Point out leukocytes.
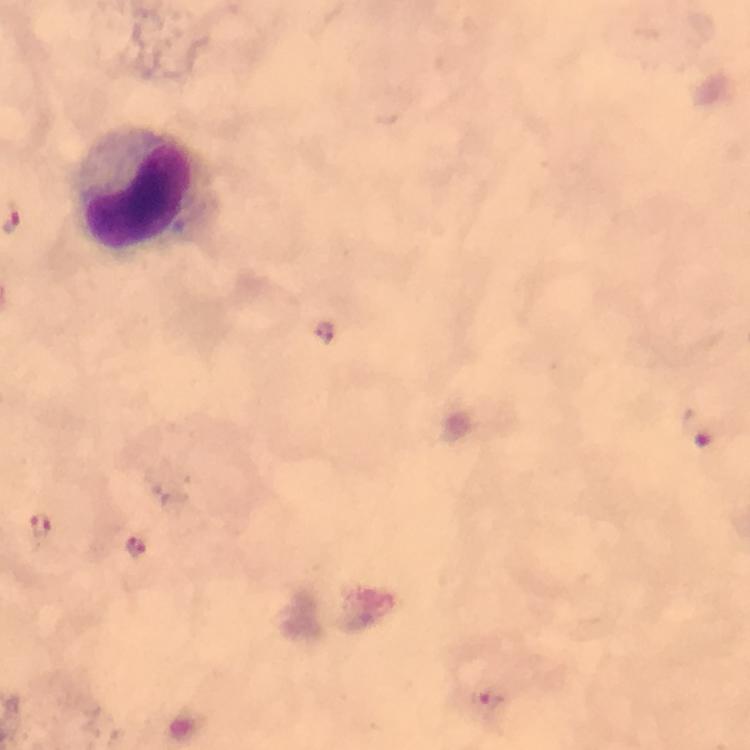
Approximate object centers, in pixels from the top-left corner.
Leukocytes: (x=147, y=189).

Plasmodium parasite locations: (x=322, y=330), (x=699, y=429), (x=42, y=527), (x=134, y=545), (x=494, y=704). Giemsa stain. Thick smear. Immersion oil applied. Image is 750×750 pixels. Cropped region of a single field of view. 100x magnification. Photographed through the microscope with a smartphone camera. From a malaria diagnostic workup.